Locate every leukocyte (white blood cell).
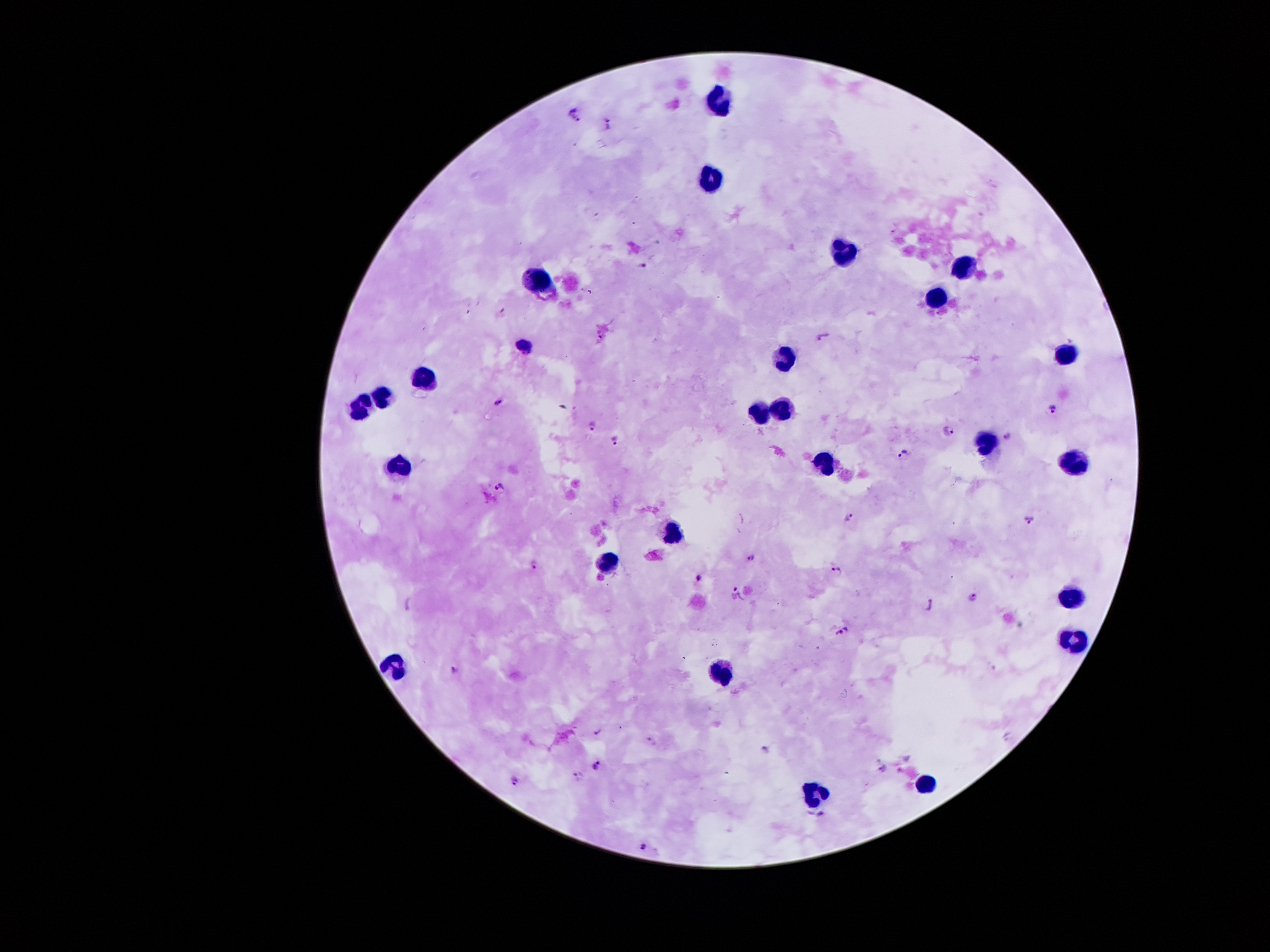
Approximate centers as (x, y) in pixels.
Leukocytes: (716, 99), (713, 179), (841, 251), (961, 267), (540, 284), (935, 301), (1066, 354), (788, 356), (423, 375), (383, 399), (785, 407), (361, 410), (759, 411), (984, 443), (823, 455), (1078, 462), (397, 466), (673, 532), (607, 566), (1071, 596), (1076, 641), (395, 665), (720, 672), (925, 785), (814, 793).

Plasmodium parasite locations = (575, 116), (609, 124), (642, 265), (823, 336), (499, 402), (1051, 408), (591, 426), (948, 431), (1008, 436), (616, 440), (905, 453), (499, 486), (849, 515), (1030, 520), (749, 557), (533, 564), (837, 571), (699, 577), (737, 593), (974, 596), (407, 604), (931, 606), (843, 633), (455, 670), (598, 730), (652, 743), (766, 749), (595, 765), (883, 769), (578, 776), (515, 781), (821, 813), (645, 845)
patient malaria status = positive for Plasmodium falciparum
preparation = thick blood smear
magnification = 100x
capture = smartphone through the microscope eyepiece
image size = 1270×952 pixels
field of view = one from this slide
stain = Giemsa